Assess this cell for malaria.
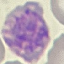
Parasitized.

Automatically extracted cell patch, resized to 64 × 64 pixels. Thin blood film. Photographed with a smartphone camera at the microscope eyepiece. Giemsa stain.